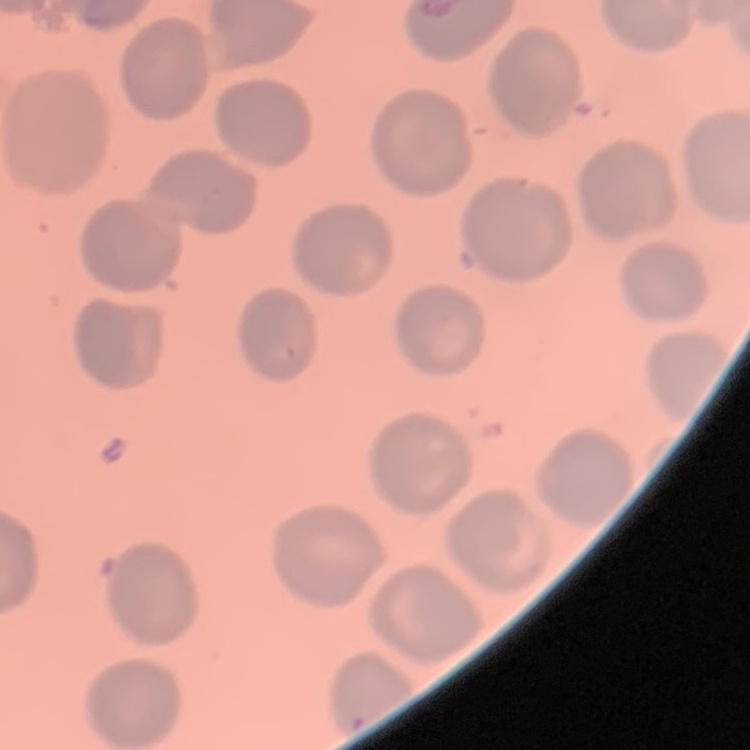

The red blood cells exhibit no rouleaux formation. Field's or Giemsa stain. One tile cut from a larger photomicrograph. Thin blood film.